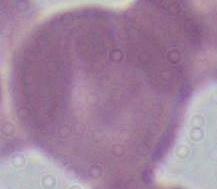

modality: photomicrograph
identification: erythrocyte
magnification: 1000x